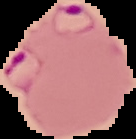
The area outside the segmented cell region is set to black. From a thin blood film. Malaria status: parasitized. Image is 136×139 pixels.